Identify the parasite.
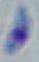

This is Toxoplasma gondii.

Summary:
  - Magnification: 1000x
  - Modality: photomicrograph